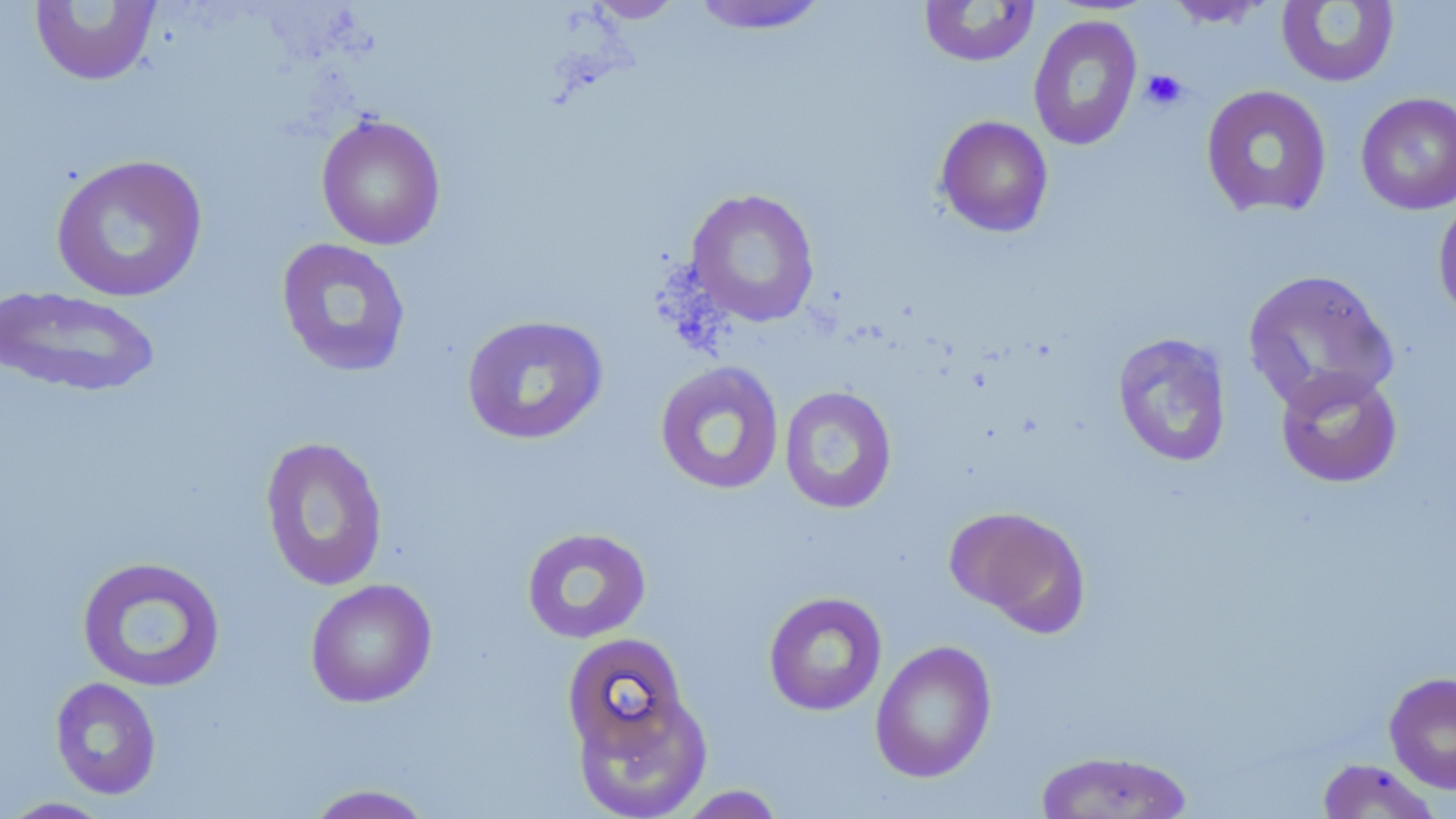
slide_level_diagnosis: no evidence of blood parasites
platelet_locations: 'approximate bounding boxes as named x1/y1/x2/y2 corners in pixels: (x1=1140, y1=69, x2=1189, y2=111)'
field_of_view: single
modality: light microscopy
stain: May-Grünwald-Giemsa
image_size: 1456×819 pixels
preparation: thin blood smear
uninfected_red_blood_cell_locations: 'approximate bounding boxes as named x1/y1/x2/y2 corners in pixels: (x1=582, y1=0, x2=688, y2=23), (x1=688, y1=0, x2=831, y2=35), (x1=29, y1=1, x2=162, y2=87), (x1=918, y1=1, x2=1040, y2=67), (x1=1162, y1=1, x2=1275, y2=28), (x1=1275, y1=1, x2=1400, y2=88), (x1=1027, y1=14, x2=1143, y2=151), (x1=1200, y1=85, x2=1333, y2=219), (x1=1355, y1=92, x2=1456, y2=215), (x1=315, y1=113, x2=446, y2=250), (x1=934, y1=116, x2=1054, y2=238), (x1=50, y1=154, x2=208, y2=303), (x1=685, y1=188, x2=821, y2=327), (x1=1433, y1=194, x2=1456, y2=326), (x1=275, y1=237, x2=412, y2=378), (x1=1242, y1=268, x2=1399, y2=413), (x1=1, y1=285, x2=162, y2=398), (x1=460, y1=314, x2=609, y2=445), (x1=1112, y1=332, x2=1233, y2=468), (x1=654, y1=361, x2=785, y2=495), (x1=1275, y1=367, x2=1403, y2=488), (x1=779, y1=385, x2=897, y2=514), (x1=259, y1=436, x2=389, y2=592), (x1=945, y1=505, x2=1091, y2=635), (x1=521, y1=526, x2=652, y2=644), (x1=75, y1=555, x2=226, y2=693), (x1=305, y1=578, x2=438, y2=708), (x1=763, y1=591, x2=888, y2=716), (x1=561, y1=632, x2=691, y2=762), (x1=870, y1=640, x2=997, y2=783), (x1=1384, y1=671, x2=1456, y2=794), (x1=49, y1=677, x2=162, y2=800), (x1=571, y1=689, x2=713, y2=818), (x1=1033, y1=750, x2=1194, y2=819), (x1=1315, y1=759, x2=1442, y2=818), (x1=300, y1=783, x2=439, y2=819), (x1=671, y1=785, x2=788, y2=818), (x1=1, y1=796, x2=115, y2=818)'
magnification: 1000x